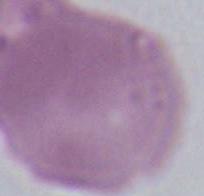

Captured at 1000x magnification. Micrograph. An erythrocyte is shown.